Classify this cell by malaria status.
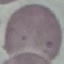
Uninfected.

Thin blood smear. Photographed with a smartphone camera at the microscope eyepiece. Cell patch, automatically extracted from a larger field of view and resized to 64 × 64 pixels. Giemsa stain.